Report the malaria status of this cell.
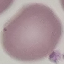
Uninfected.

Summary:
  - Capture: smartphone camera at the microscope eyepiece
  - Stain: Giemsa
  - Preparation: thin blood film
  - Image type: automatically extracted cell patch, resized to 64 × 64 pixels